Assess this cell for malaria.
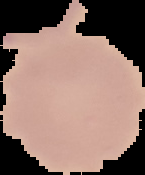

It is uninfected.

preparation = thin blood film
image size = 145×175 pixels
image type = cell region segmented out of the field of view; surrounding area masked to black